Identify the parasite.
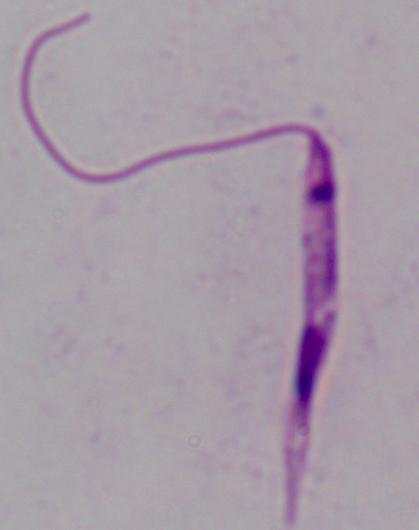
This is Leishmania.

1000x magnification. Photomicrograph.